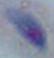

Summary:
  - Magnification: 1000x
  - Identification: Toxoplasma gondii
  - Modality: micrograph